State the blood parasite species.
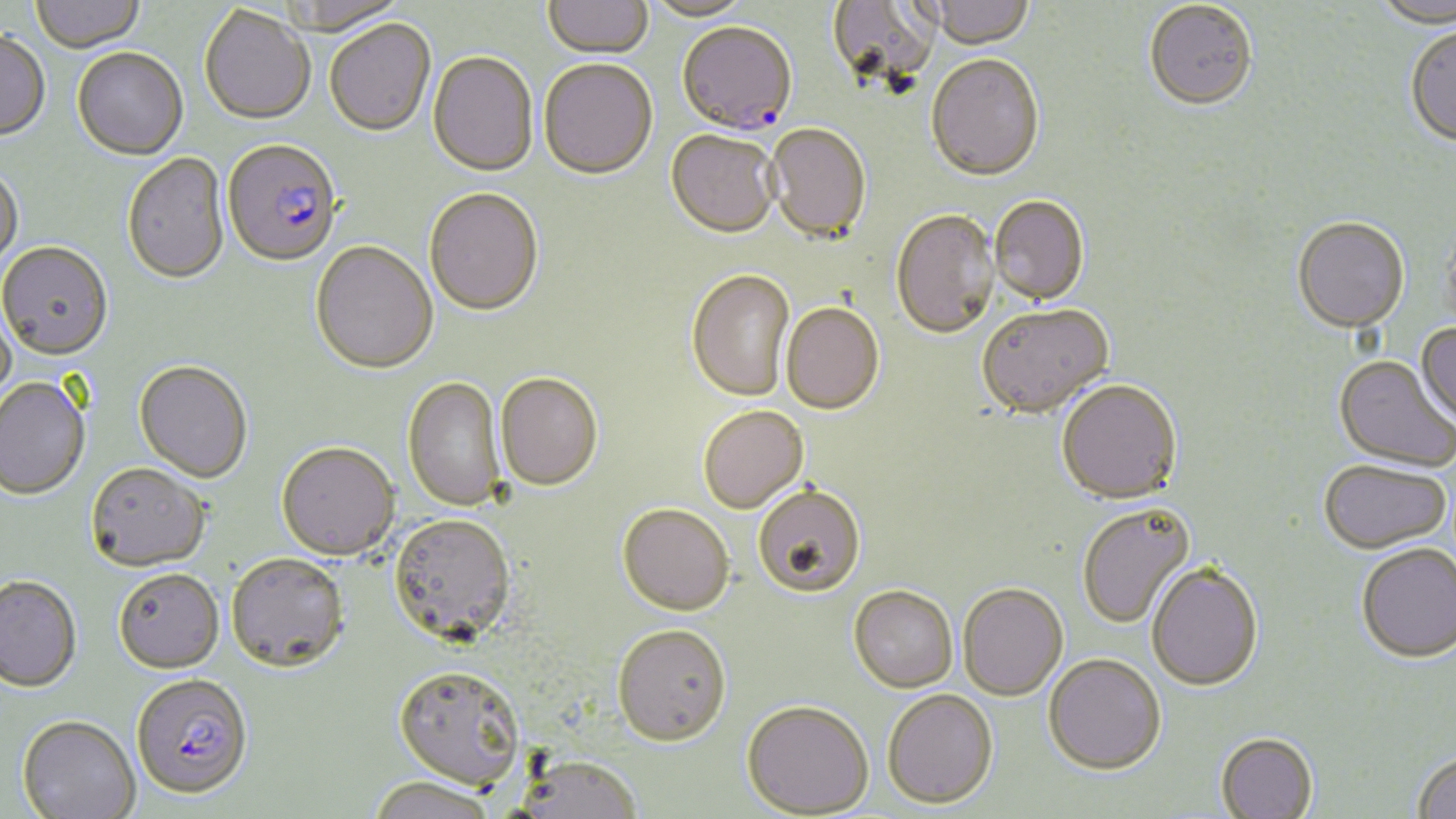
Plasmodium falciparum.

Approximate bounding boxes as (x1, y1, x2, y2) in pixels. Plasmodium falciparum-infected red blood cell locations: (677, 24, 797, 139), (222, 141, 341, 269), (131, 677, 253, 803). Uninfected red blood cell locations: (30, 0, 146, 54), (275, 0, 409, 39), (541, 0, 653, 61), (826, 0, 940, 96), (919, 0, 1037, 53), (642, 1, 758, 23), (1374, 2, 1456, 30), (1144, 3, 1258, 114), (199, 7, 316, 127), (325, 21, 436, 139), (1405, 27, 1456, 151), (0, 33, 50, 143), (73, 49, 188, 161), (428, 54, 538, 178), (926, 56, 1045, 184), (538, 61, 658, 183), (765, 126, 871, 246), (665, 132, 779, 241), (121, 154, 230, 287), (0, 167, 24, 274), (424, 190, 544, 318), (989, 197, 1089, 308), (890, 211, 1000, 342), (1292, 220, 1409, 336), (1441, 222, 1456, 340), (311, 243, 438, 376), (0, 244, 113, 363), (686, 271, 796, 403), (0, 303, 16, 414), (781, 304, 884, 417), (977, 306, 1114, 421), (1415, 323, 1456, 430), (1333, 357, 1455, 474), (134, 362, 253, 484), (495, 374, 603, 493), (403, 378, 507, 513), (0, 379, 91, 501), (1056, 382, 1183, 508), (699, 407, 809, 514), (276, 444, 399, 563), (1318, 463, 1452, 557), (86, 464, 210, 574), (753, 487, 865, 600), (618, 505, 734, 617), (1077, 505, 1196, 630), (388, 516, 516, 648), (1356, 546, 1456, 667), (226, 555, 350, 676), (1147, 565, 1264, 693), (114, 570, 224, 675), (0, 578, 82, 695), (958, 585, 1068, 703), (848, 587, 958, 694), (611, 626, 731, 749), (1043, 656, 1166, 778), (393, 667, 525, 792), (882, 691, 999, 811), (740, 702, 873, 818), (16, 718, 141, 819), (1215, 735, 1318, 819), (1411, 754, 1456, 819), (515, 758, 643, 818), (367, 778, 498, 819). One field of a larger specimen. Image is 1456×819 pixels. Optical microscopy. Captured at 1000x magnification. Thin blood smear. May-Grünwald-Giemsa-stained preparation.